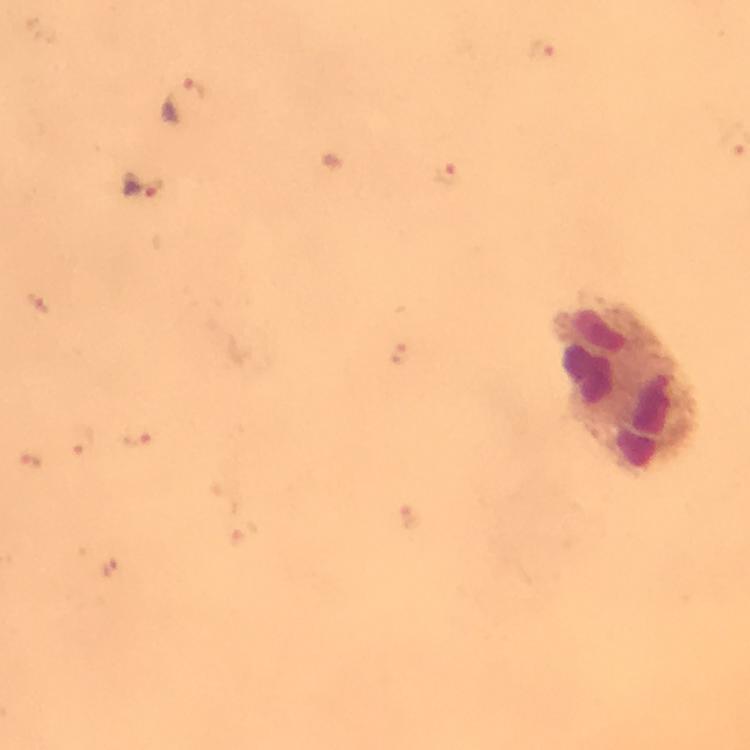
Approximate centers as (x, y) in pixels. Leukocyte locations: (625, 388). Plasmodium parasite locations: (183, 102), (142, 186). From a diagnostic examination for malaria. Image is 750×750 pixels. Immersion oil applied. Photographed through the microscope with a smartphone camera. Cropped region of a single field of view. 100x magnification. Thick blood film. Giemsa-stained preparation.